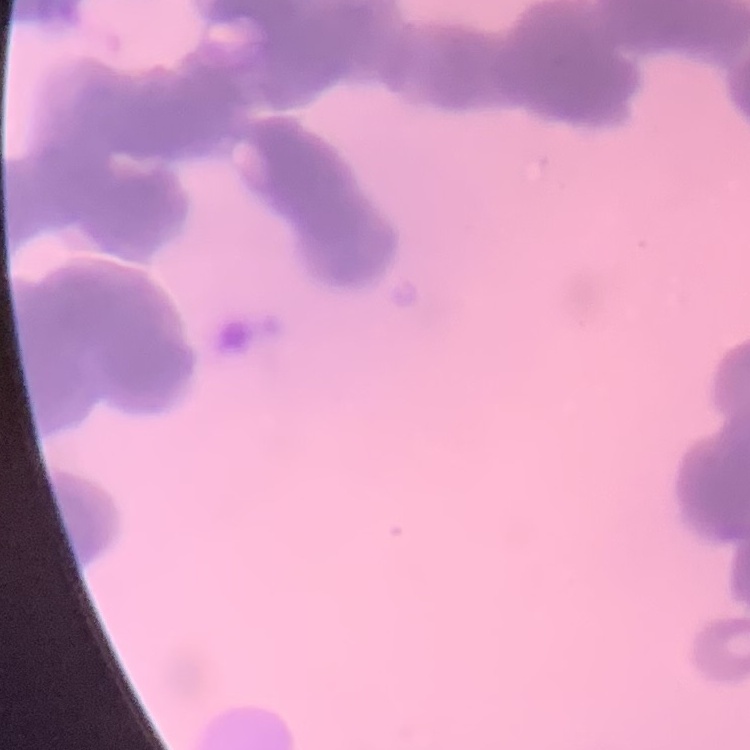
Summary:
  - Erythrocyte morphology: rouleaux formation
  - Stain: Field's or Giemsa
  - Image type: square crop of a larger photomicrograph
  - Preparation: thin blood smear